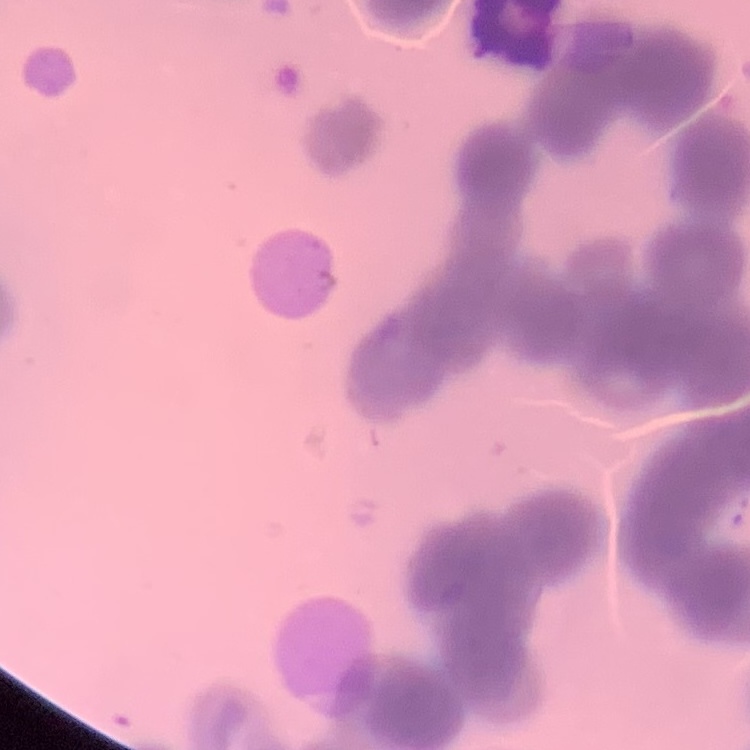
Summary:
  - Red blood cell morphology: rouleaux formation
  - Image type: one tile cut from a larger photomicrograph
  - Preparation: thin peripheral smear
  - Stain: Field's or Giemsa